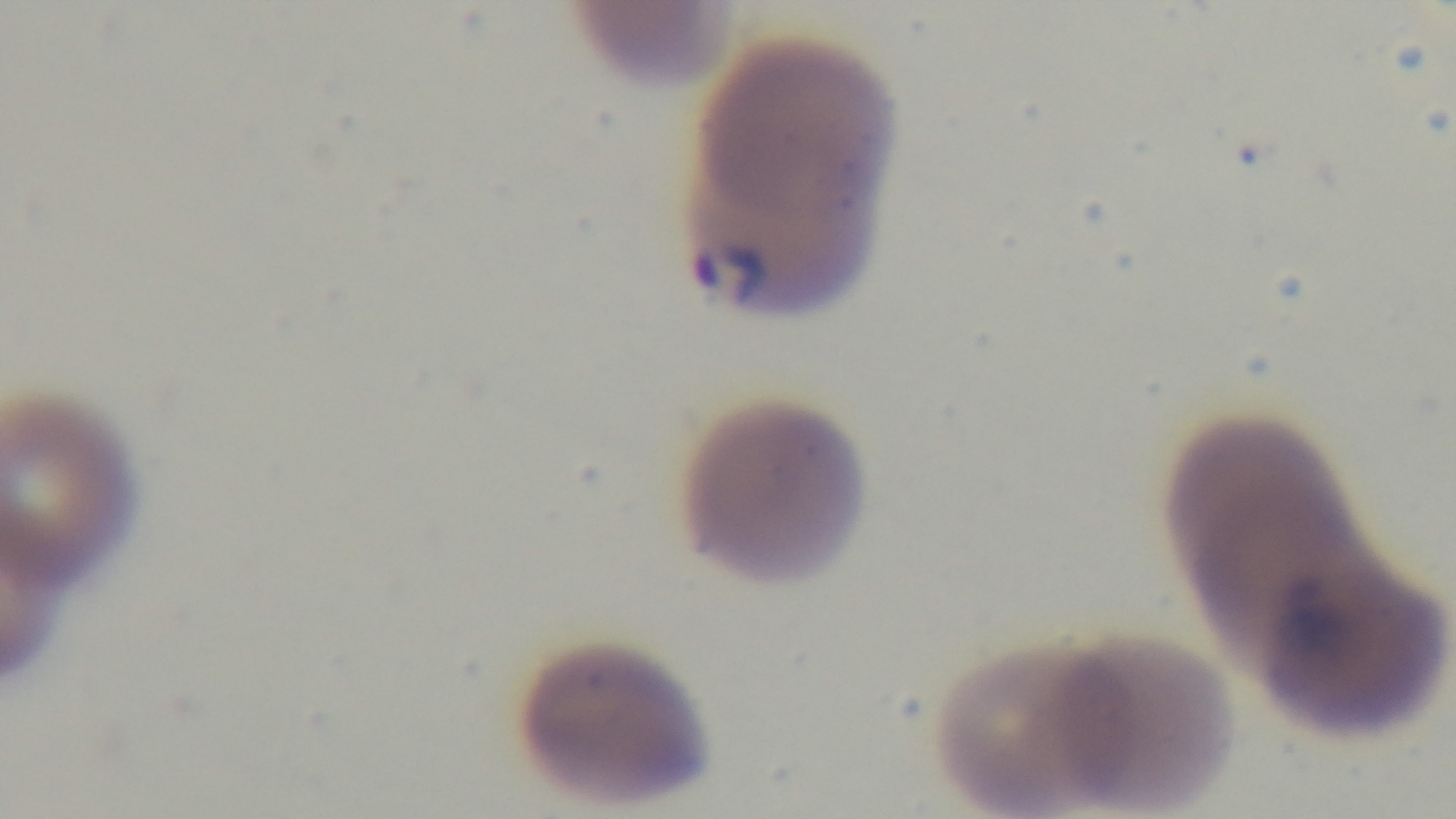
capture: mounted 4K digital camera
preparation: thin
objective: 100x oil immersion
modality: light microscopy
field_of_view: one from the slide
malaria_status: infected
stain: Giemsa